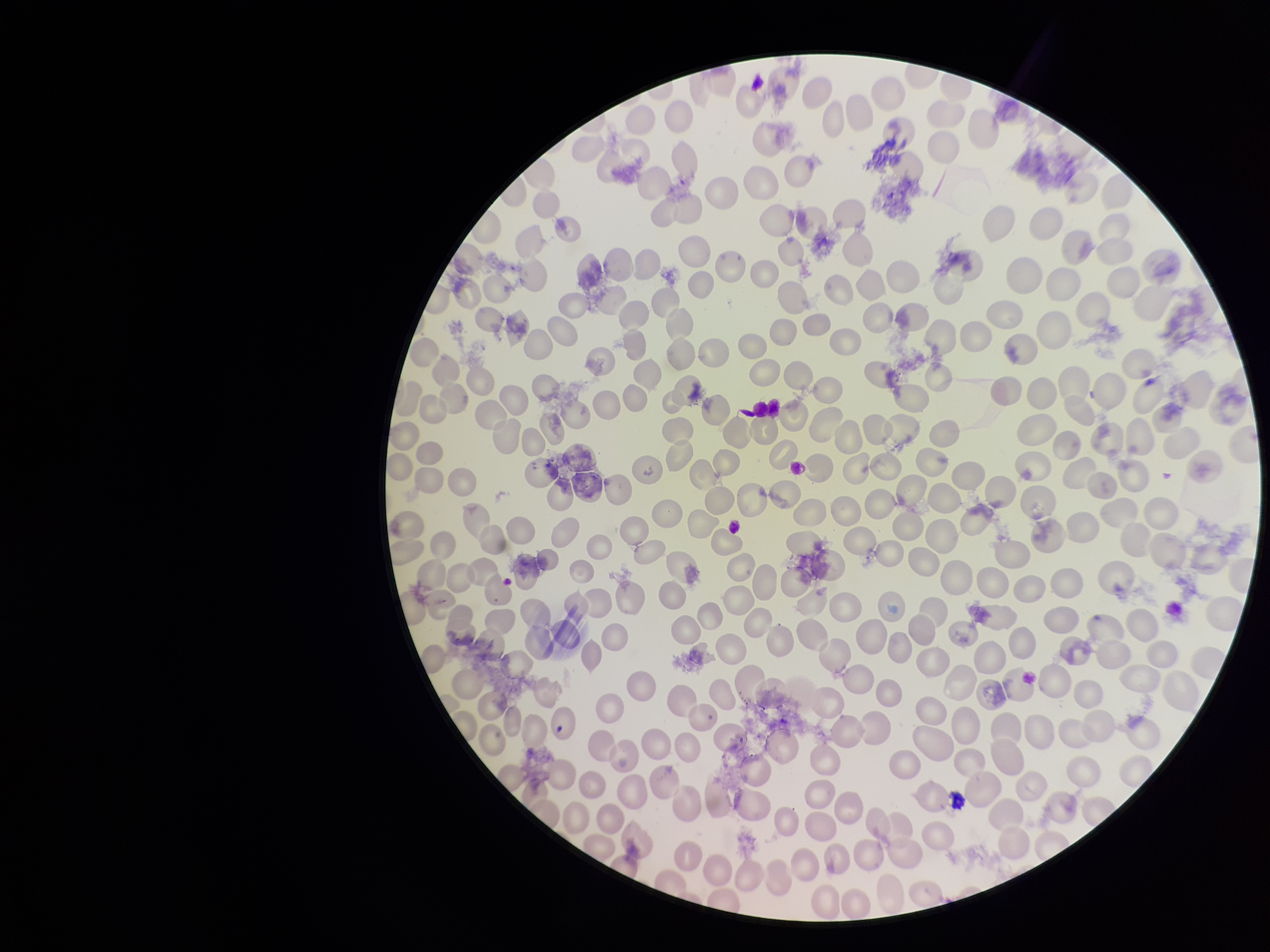
Preparation: thin blood smear. Giemsa stain. Red blood cell count: 268. Smartphone photograph taken through the eyepiece of a microscope. Species reported for this patient: Plasmodium falciparum. Patient malaria status: positive. Image is 1270×952 pixels. Parasitized red blood cell count: 0. Parasitized red blood cells: none identified. One field from this slide.